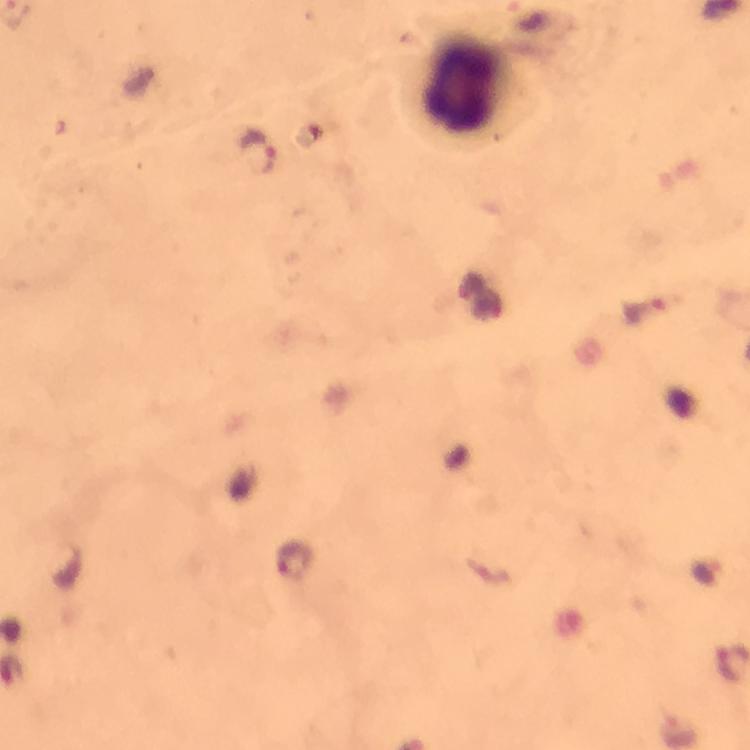

context = from a malaria diagnostic workup
leukocyte locations = approximate centers as (x, y) in pixels: (468, 86)
stain = Giemsa
immersion oil = used
capture = smartphone photograph through a microscope
preparation = thick smear
image size = 750×750 pixels
Plasmodium parasite locations = approximate centers as (x, y) in pixels: (258, 152), (296, 558)
magnification = 100x
cropped from = one field of view